State which cell type is depicted.
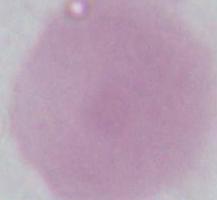

This is an erythrocyte.

modality: micrograph
magnification: 1000x